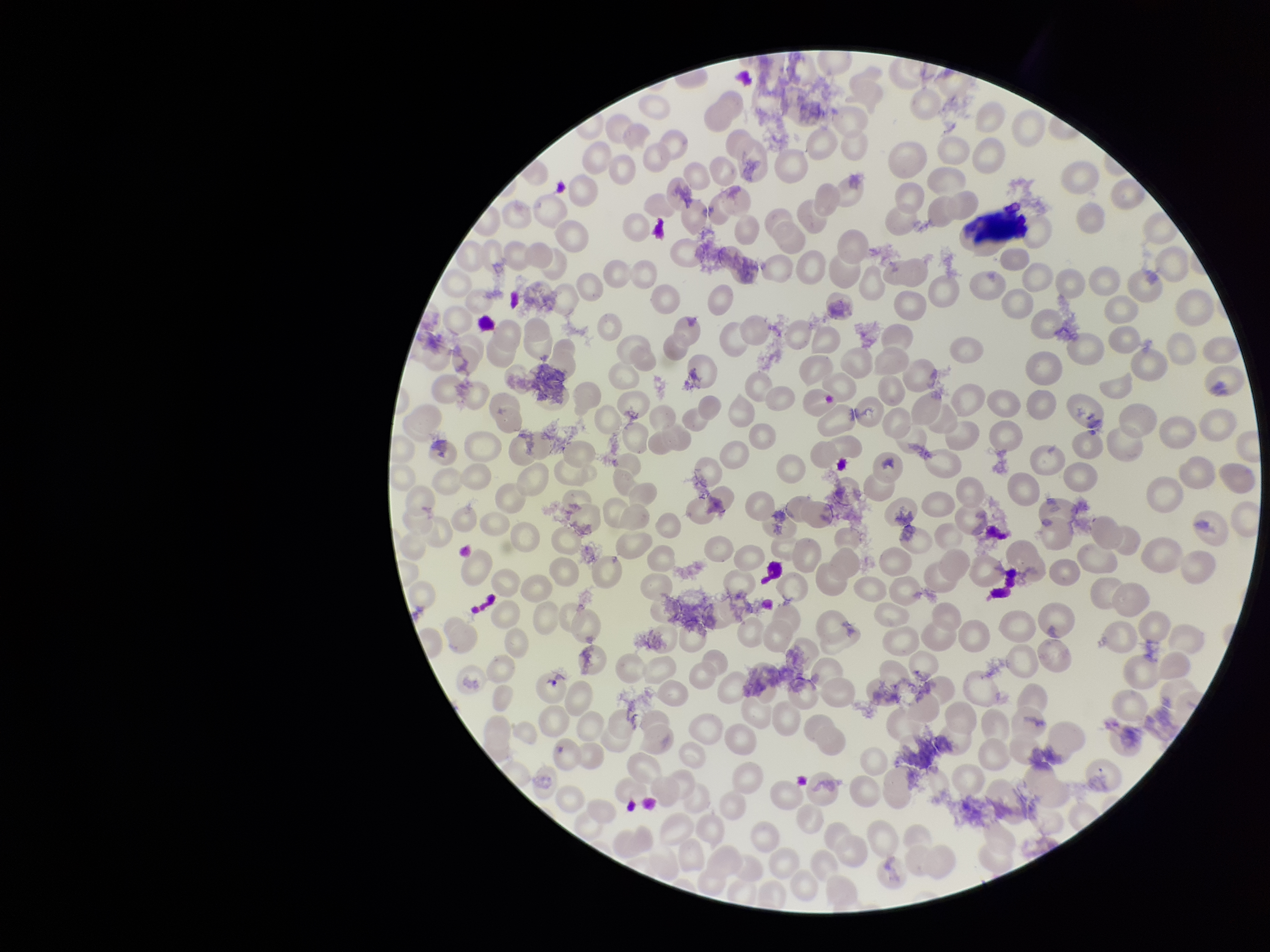

preparation: thin smear
parasitized_red_blood_cell_count: 0
field_of_view: single
capture: smartphone photograph through the microscope eyepiece
stain: Giemsa
red_blood_cell_count: 233
patient_malaria_status: negative
image_size: 1270×952 pixels
parasitized_red_blood_cells: none seen